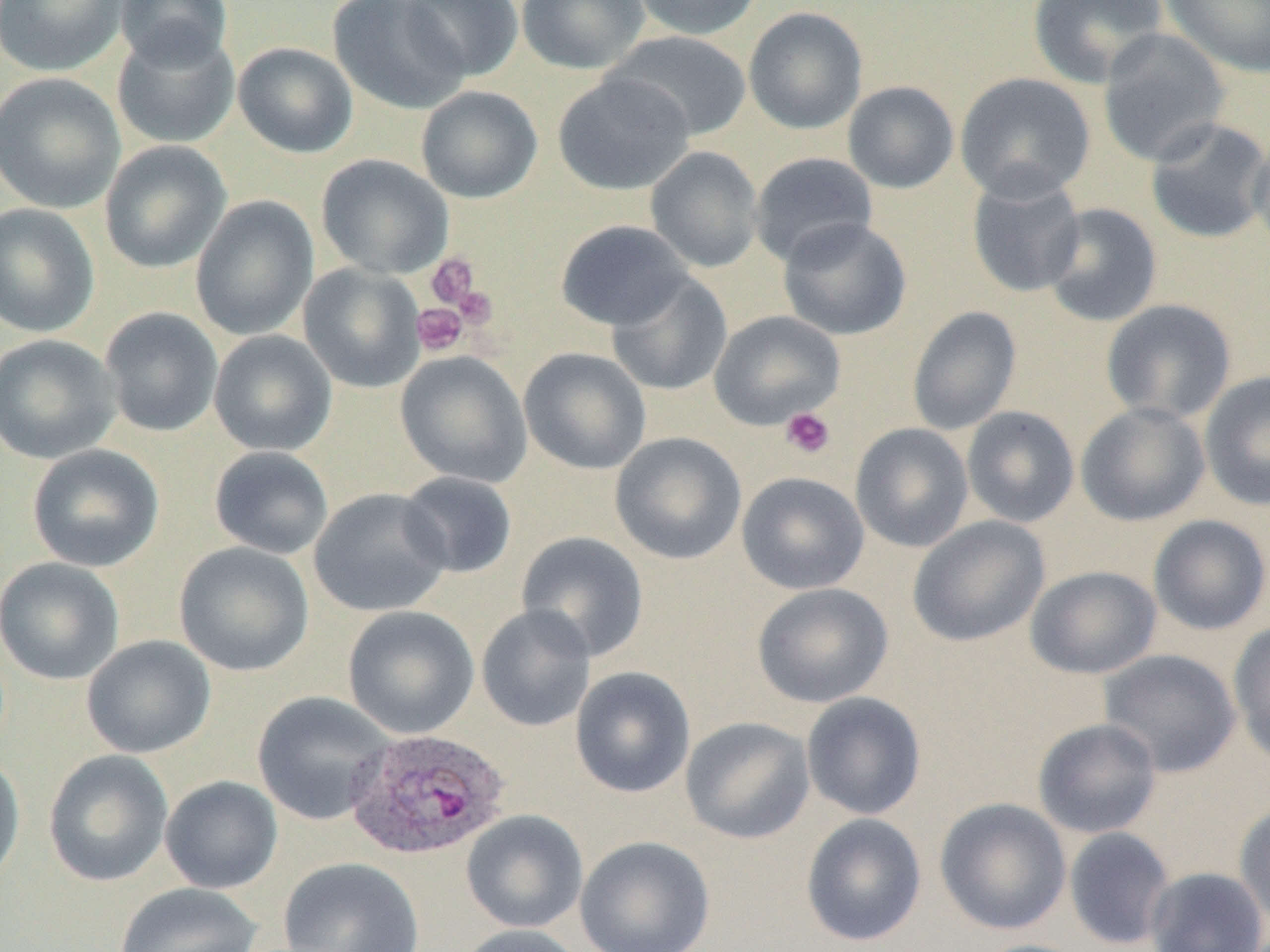
Approximate bounding boxes as (x1, y1, x2, y2) in pixels. Platelet locations: (425, 252, 480, 310), (453, 285, 498, 329), (411, 303, 467, 356), (780, 407, 836, 460). Uninfected red blood cell locations: (0, 0, 130, 77), (114, 0, 234, 69), (328, 0, 470, 114), (400, 0, 524, 81), (516, 0, 650, 74), (627, 0, 763, 41), (1027, 0, 1168, 89), (1161, 0, 1270, 78), (743, 6, 867, 135), (112, 25, 241, 149), (1097, 28, 1231, 167), (604, 31, 752, 141), (233, 41, 358, 159), (0, 72, 126, 214), (553, 72, 695, 195), (955, 72, 1096, 203), (842, 81, 959, 194), (416, 85, 542, 203), (1145, 117, 1270, 244), (1249, 131, 1270, 258), (99, 140, 232, 274), (645, 146, 764, 273), (749, 152, 878, 268), (316, 153, 454, 279), (966, 173, 1087, 298), (190, 195, 319, 341), (0, 203, 100, 337), (1042, 203, 1162, 328), (778, 217, 912, 340), (556, 220, 693, 331), (298, 263, 427, 393), (605, 271, 733, 396), (1101, 299, 1237, 424), (907, 305, 1022, 435), (99, 307, 224, 437), (708, 310, 847, 430), (208, 330, 337, 457), (0, 333, 121, 464), (519, 347, 652, 476), (395, 351, 532, 488), (1200, 370, 1270, 511), (1076, 401, 1210, 527), (961, 405, 1080, 528), (850, 423, 973, 552), (610, 432, 746, 565), (26, 444, 165, 572), (208, 446, 334, 559), (397, 471, 518, 579), (736, 471, 869, 594), (308, 487, 452, 618), (1148, 514, 1270, 635), (908, 516, 1050, 647), (515, 531, 649, 662), (173, 542, 315, 677), (0, 557, 124, 685), (1025, 565, 1161, 679), (751, 582, 894, 708), (475, 604, 596, 732), (342, 605, 480, 739), (1228, 620, 1270, 765), (81, 635, 216, 759), (1099, 649, 1241, 777), (570, 666, 696, 798), (252, 690, 396, 826), (801, 692, 926, 820), (680, 716, 816, 844), (1032, 718, 1162, 839), (43, 749, 174, 887), (0, 752, 25, 890), (160, 775, 283, 894), (934, 797, 1072, 935), (1234, 801, 1270, 929), (461, 809, 588, 933), (800, 813, 927, 947), (1064, 827, 1176, 950), (575, 835, 715, 952), (278, 857, 425, 952), (1145, 867, 1269, 952), (111, 882, 264, 952), (455, 924, 585, 952). Plasmodium ovale-infected red blood cell locations: (345, 727, 511, 861). Slide-level diagnosis: Plasmodium ovale. Single field of view. Thin blood smear. Captured at 1000x magnification. Optical microscopy. Image is 1270×952 pixels.